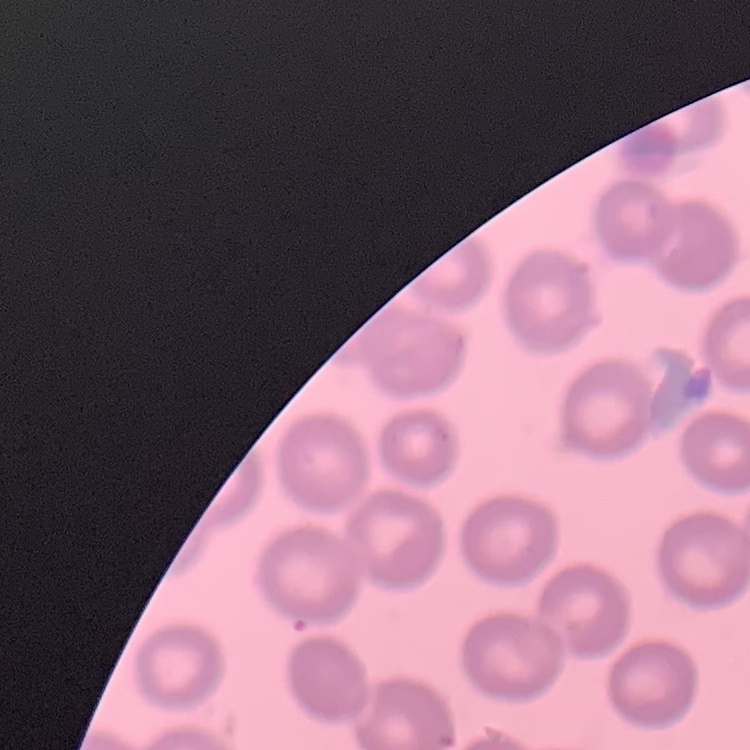
Summary:
  - Red blood cell morphology: no rouleaux formation
  - Image type: one tile cut from a larger photomicrograph
  - Preparation: thin peripheral smear
  - Stain: Field's or Giemsa